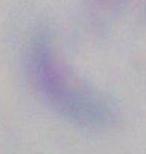
Summary:
  - Modality: micrograph
  - Magnification: 1000x
  - Identification: Toxoplasma gondii